Locate the cells, classifying each as a parasitized red blood cell, an uninfected red blood cell, or a white blood cell.
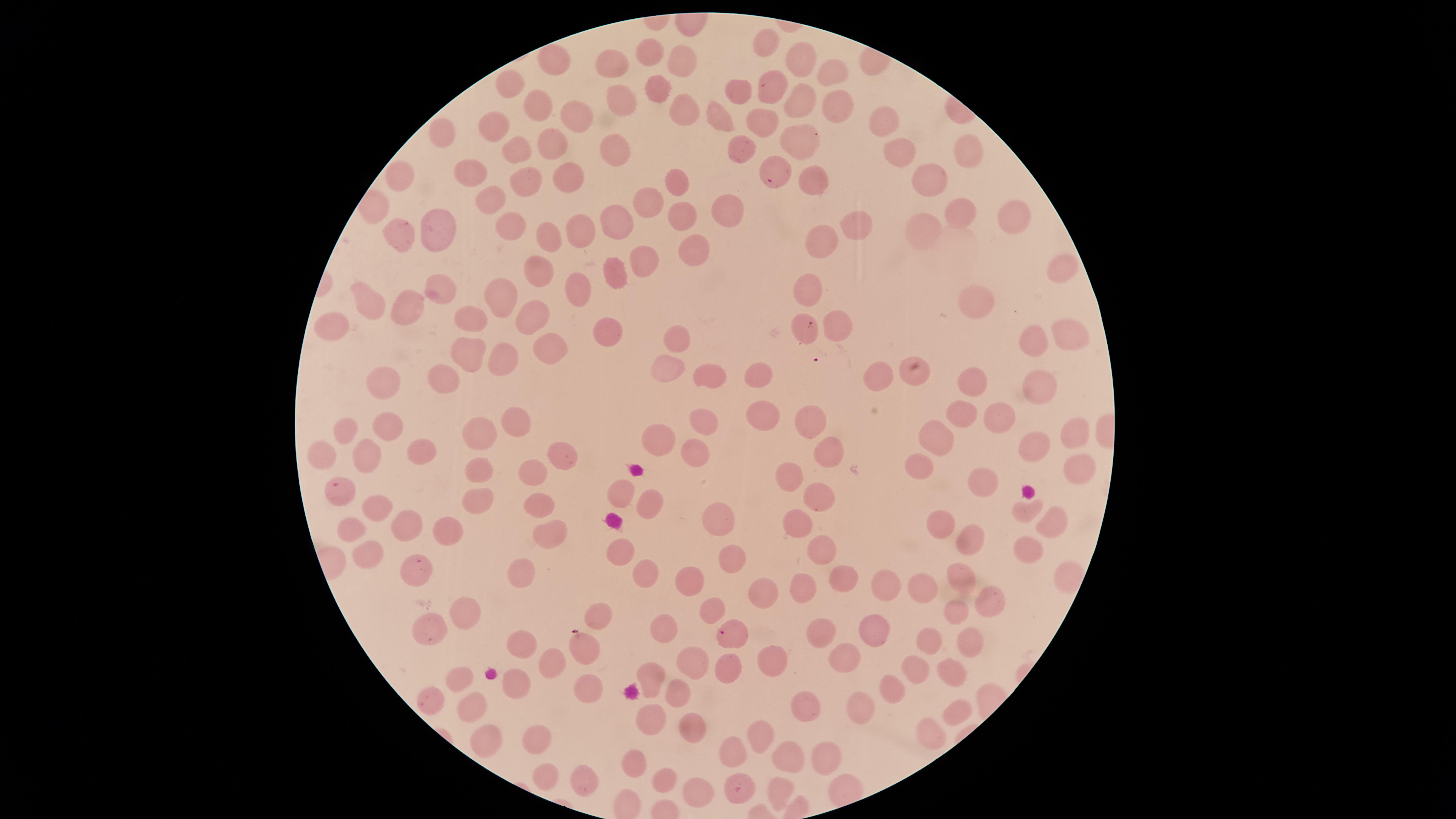
Approximate marker points as [x, y] in pixels.
Parasitized red blood cells: [770, 181], [811, 325], [342, 492], [417, 566], [722, 632], [738, 790].
Uninfected red blood cells: [767, 47], [650, 58], [550, 61], [801, 61], [680, 62], [616, 67], [831, 73], [510, 84], [772, 86], [736, 89], [656, 93], [793, 100], [536, 101], [623, 105], [832, 106], [679, 110], [573, 119], [884, 119], [716, 126], [760, 127], [496, 128], [443, 133], [802, 136], [554, 142], [969, 147], [742, 148], [516, 150], [899, 150], [616, 153], [469, 166], [568, 178], [813, 179], [676, 180], [397, 182], [525, 182], [928, 182], [492, 200], [649, 205], [725, 205], [959, 217], [682, 219], [616, 222], [1011, 222], [856, 224], [508, 227], [433, 230], [577, 233], [921, 233], [393, 236], [552, 240], [827, 243], [697, 252], [640, 259], [1063, 268], [541, 270], [614, 274], [435, 287], [576, 288], [808, 290], [501, 299], [978, 299], [364, 305], [405, 305], [532, 312], [471, 319], [330, 327], [837, 327], [611, 333], [1069, 335], [671, 340], [1028, 340], [550, 347], [468, 353], [503, 357], [669, 368], [711, 375], [914, 375], [878, 377], [757, 378], [447, 380], [973, 381], [1040, 382], [381, 386], [961, 412], [994, 416], [704, 419], [762, 419], [514, 420], [813, 420], [389, 426], [345, 432], [481, 433], [1068, 434], [660, 436], [939, 440], [1029, 447], [419, 451], [693, 452], [829, 453], [366, 454], [322, 455], [561, 455], [917, 462], [482, 466], [533, 474], [1073, 475], [790, 480], [979, 485], [820, 492], [622, 494], [482, 498], [648, 500], [539, 503], [375, 507], [1024, 510], [790, 521], [717, 522], [407, 523], [941, 523], [1049, 523], [550, 526], [449, 529], [351, 530], [966, 544], [819, 547], [619, 549], [1028, 552], [369, 557], [729, 560], [641, 567], [522, 574], [841, 578], [961, 579], [687, 580], [890, 584], [923, 586], [803, 589], [762, 590], [985, 603], [712, 610], [955, 610], [459, 611], [602, 615], [661, 626], [871, 629], [429, 631], [820, 633], [925, 641], [521, 643], [585, 643], [968, 644], [843, 657], [553, 660], [692, 660], [769, 663], [724, 668], [915, 668], [951, 673], [651, 676], [458, 679], [590, 681], [518, 683], [890, 688], [673, 694], [429, 696], [473, 705], [804, 705], [854, 707], [960, 715], [649, 717], [692, 727], [931, 732], [762, 735], [482, 739], [535, 743], [730, 753], [788, 755], [823, 757], [632, 764], [664, 776], [545, 778], [583, 778], [777, 786], [698, 791].
No white blood cells identified.

{
  "visible_region": "circular",
  "image_size": "1456×819 pixels",
  "preparation": "thin smear of blood",
  "capture": "smartphone photograph through the microscope eyepiece",
  "species": "Plasmodium falciparum",
  "field_of_view": "single",
  "stain": "Giemsa"
}